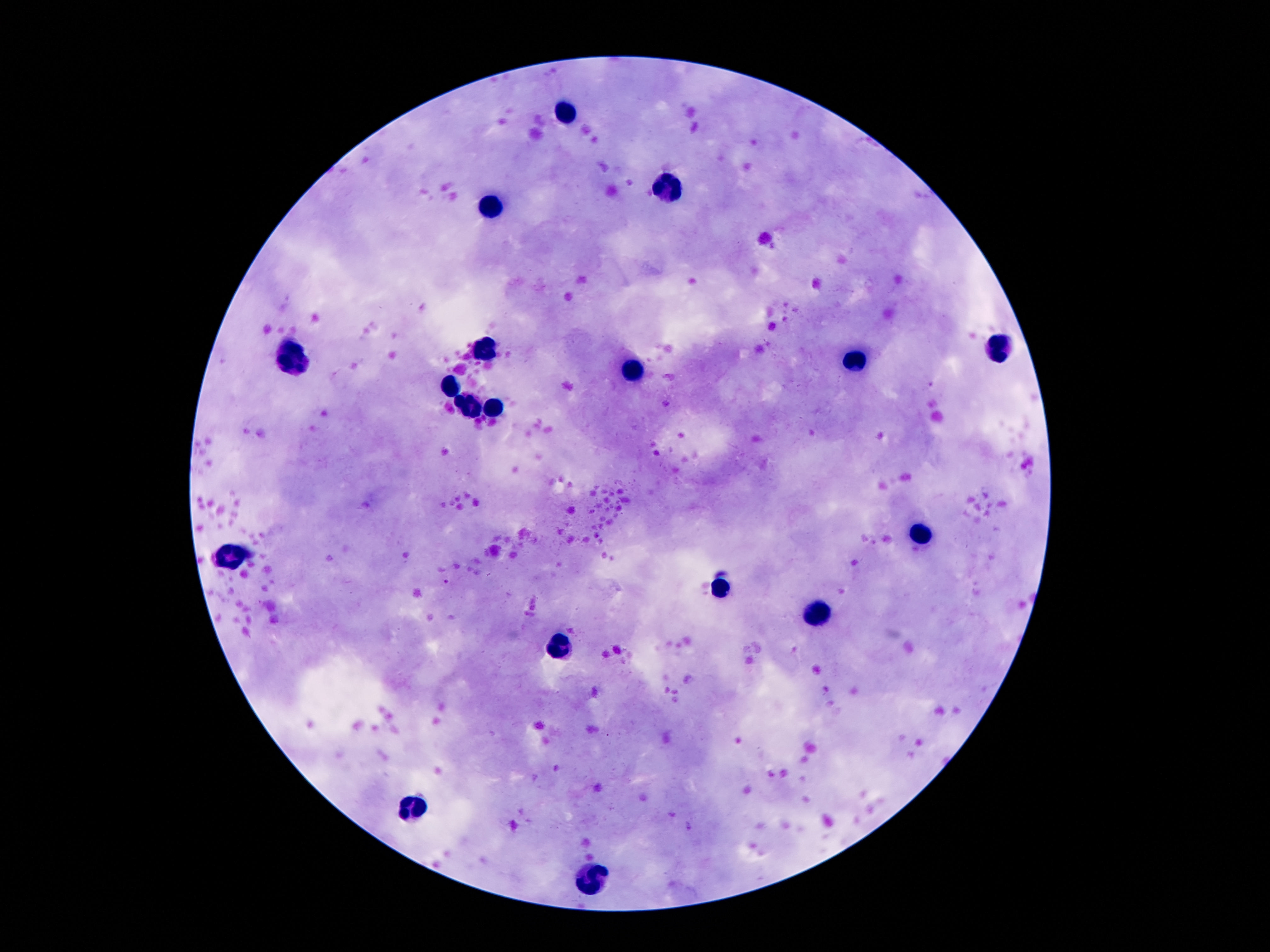
Approximate object centers, in pixels from the top-left corner. Leukocyte locations: (x=566, y=111), (x=668, y=189), (x=492, y=209), (x=486, y=346), (x=1000, y=350), (x=290, y=358), (x=858, y=360), (x=630, y=370), (x=450, y=390), (x=474, y=406), (x=496, y=410), (x=922, y=536), (x=230, y=556), (x=720, y=588), (x=818, y=614), (x=562, y=646), (x=420, y=810), (x=592, y=882). Thick peripheral-blood smear. Smartphone photograph taken through the microscope eyepiece. Giemsa-stained preparation. Single field of view. Image is 1270×952 pixels. 100x magnification. Patient malaria status: negative.